Name the parasite shown.
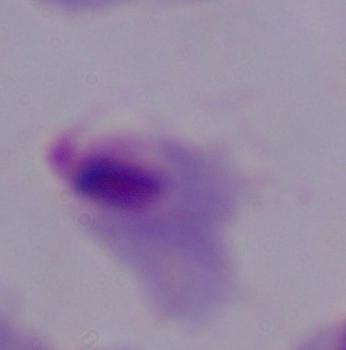
This is a trichomonad.

1000x magnification. Micrograph.